Identify the parasite.
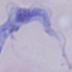
A trypanosome.

Captured at 1000x magnification. Photomicrograph.